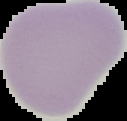
Result: negative for Plasmodium parasites. Cell region segmented out of the field of view; the surrounding area is masked to black. Image is 127×121 pixels. From a thin blood smear.